Point out each Plasmodium parasite.
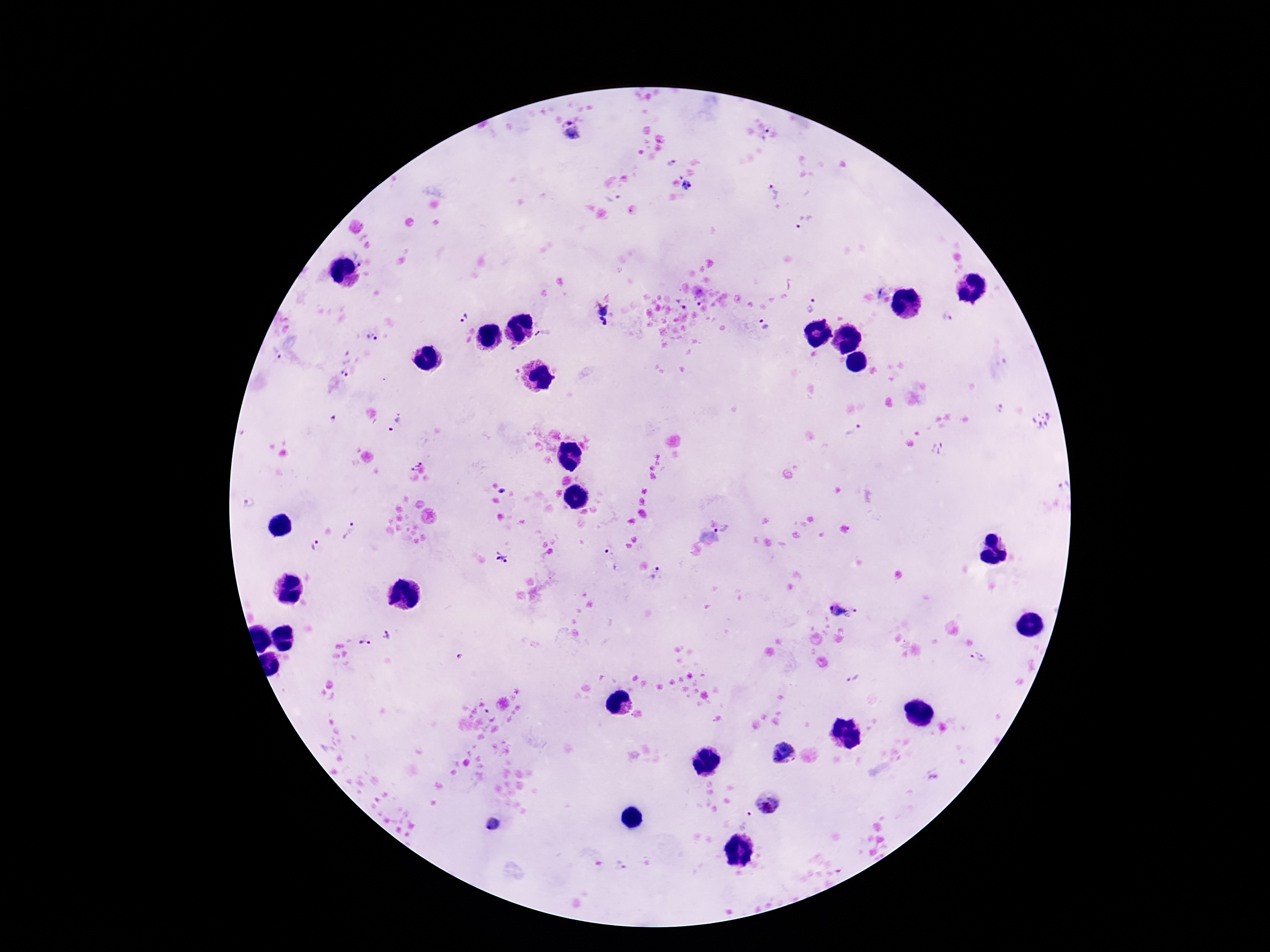

Approximate object centers, in pixels from the top-left corner.
Plasmodium parasites: (x=571, y=132), (x=766, y=137), (x=670, y=163), (x=689, y=187), (x=773, y=191), (x=802, y=221), (x=359, y=257), (x=702, y=301), (x=684, y=303), (x=812, y=304), (x=599, y=312), (x=463, y=317), (x=947, y=317), (x=765, y=325), (x=543, y=333), (x=371, y=339), (x=274, y=352), (x=344, y=364), (x=1000, y=411), (x=331, y=417), (x=1043, y=420), (x=395, y=424), (x=854, y=431), (x=939, y=448), (x=414, y=464), (x=1064, y=484), (x=502, y=490), (x=249, y=505), (x=723, y=529), (x=353, y=533), (x=317, y=546), (x=609, y=553), (x=502, y=558), (x=656, y=574), (x=839, y=610), (x=387, y=635), (x=365, y=642), (x=978, y=657), (x=853, y=678), (x=489, y=711), (x=786, y=754), (x=770, y=803), (x=747, y=820), (x=494, y=824), (x=620, y=865).

Summary:
  - Field of view: one from this slide
  - Magnification: 100x
  - Stain: Giemsa
  - Capture: smartphone camera through the microscope eyepiece
  - Preparation: thick blood film
  - Image size: 1270×952 pixels
  - Patient malaria status: infected